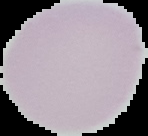
Result: no Plasmodium parasites seen. The area outside the segmented cell region is set to black. From a thin blood smear. Image is 148×136 pixels.